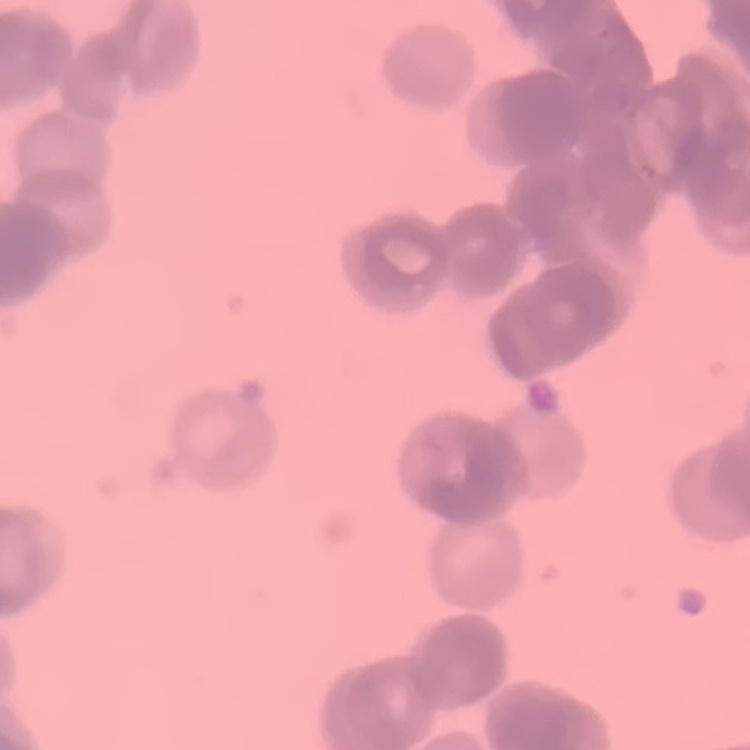 The erythrocytes exhibit rouleaux formation. Field's or Giemsa stain. Square crop of a larger photomicrograph. Thin peripheral smear.